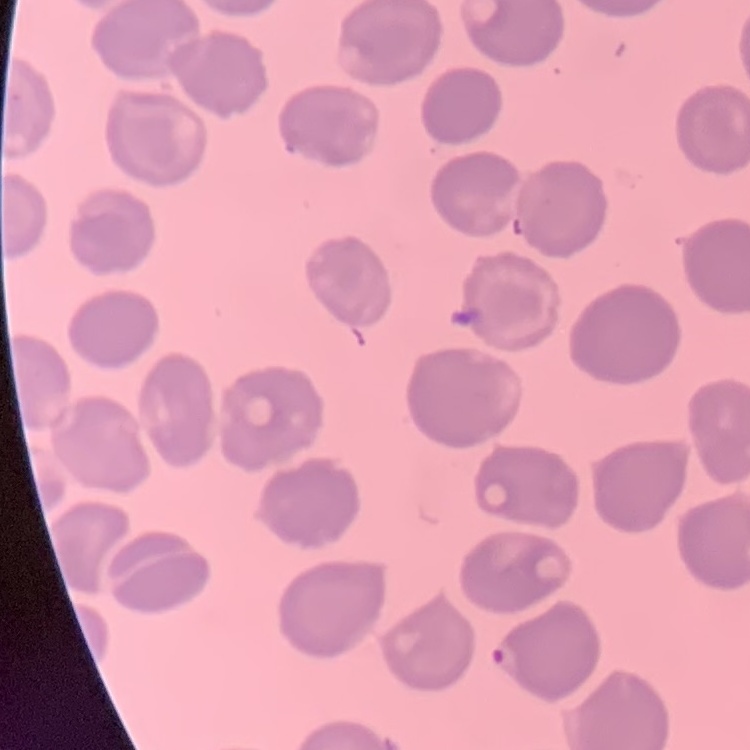

red_blood_cell_morphology: no rouleaux formation
stain: Field's or Giemsa
image_type: one tile cut from a larger photomicrograph
preparation: thin blood film